Identify the cell.
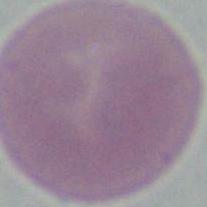

This is an erythrocyte.

Captured at 1000x magnification. Micrograph.